Describe the morphology of the red blood cells.
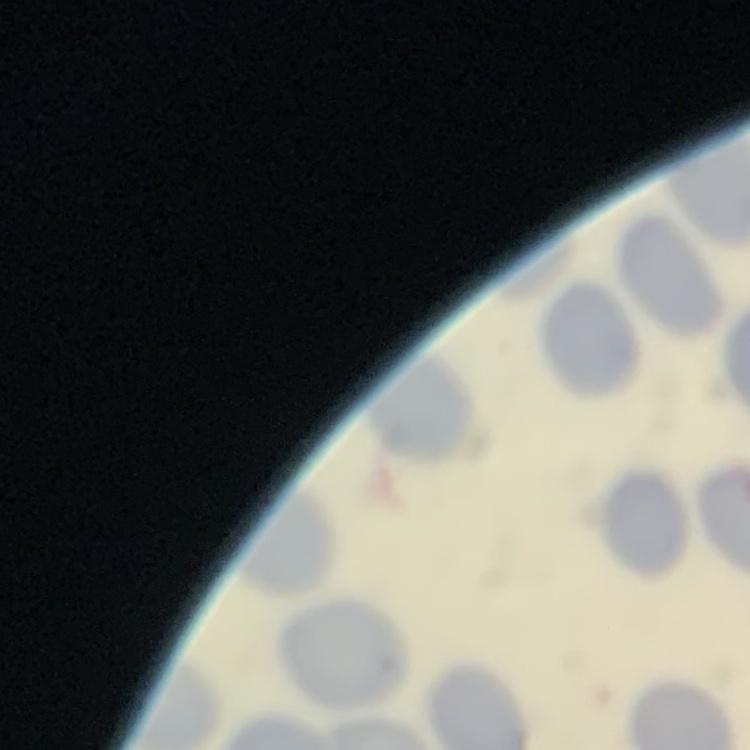
They show no rouleaux formation.

One tile cut from a larger photomicrograph. Thin blood film. Field's or Giemsa stain.